Locate every blood parasite and identify its species.
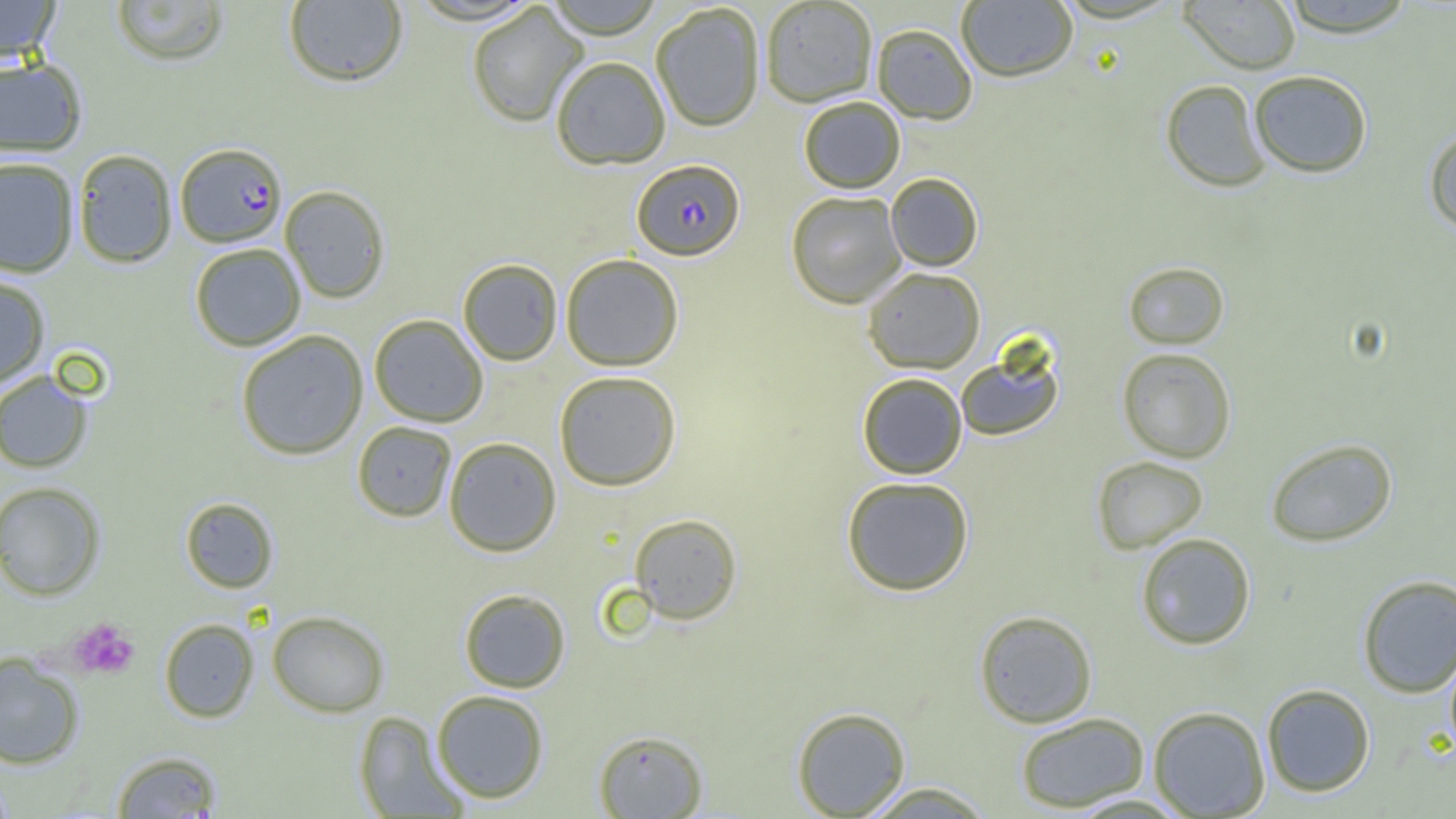

Approximate bounding boxes as (x1, y1, x2, y2) in pixels.
Plasmodium falciparum-infected red blood cells: (175, 142, 287, 248), (632, 159, 745, 260).
No Plasmodium ovale, Plasmodium malariae, Plasmodium vivax, Babesia divergens, or Trypanosoma brucei observed.

Summary:
  - Platelet locations: (69, 617, 139, 679)
  - Uninfected red blood cell locations: (0, 0, 61, 65), (542, 0, 665, 38), (1180, 0, 1302, 74), (1277, 0, 1419, 37), (110, 1, 230, 66), (283, 1, 408, 87), (760, 1, 878, 107), (956, 1, 1077, 82), (467, 3, 588, 128), (650, 3, 766, 132), (871, 23, 978, 124), (550, 55, 671, 170), (0, 56, 88, 158), (1248, 70, 1373, 178), (1160, 79, 1271, 192), (798, 96, 905, 193), (1423, 126, 1456, 233), (72, 149, 177, 268), (0, 157, 79, 278), (885, 173, 984, 271), (280, 185, 390, 303), (786, 191, 906, 308), (190, 243, 306, 351), (560, 253, 684, 371), (457, 258, 563, 365), (1123, 261, 1229, 349), (862, 267, 986, 374), (0, 273, 50, 387), (369, 314, 488, 427), (235, 330, 369, 460), (955, 348, 1064, 441), (1117, 348, 1236, 462), (554, 370, 682, 491), (0, 371, 94, 473), (857, 372, 967, 479), (352, 421, 457, 522), (444, 437, 562, 556), (1265, 438, 1397, 547), (1091, 455, 1208, 554), (841, 476, 974, 596), (0, 481, 105, 601), (180, 497, 278, 593), (629, 513, 743, 625), (1135, 532, 1256, 650), (1357, 573, 1456, 698), (458, 588, 571, 693), (974, 610, 1098, 728), (267, 611, 389, 717), (159, 618, 259, 722), (1443, 643, 1456, 762), (0, 652, 85, 770), (1261, 683, 1375, 797), (431, 690, 549, 804), (791, 706, 911, 817), (1147, 706, 1271, 818), (354, 710, 467, 817), (1015, 712, 1150, 813), (593, 729, 707, 818), (112, 750, 223, 818), (858, 782, 996, 818)
  - Slide-level diagnosis: Plasmodium falciparum
  - Image size: 1456×819 pixels
  - Preparation: thin blood film
  - Field of view: single
  - Modality: light microscopy
  - Magnification: 1000x